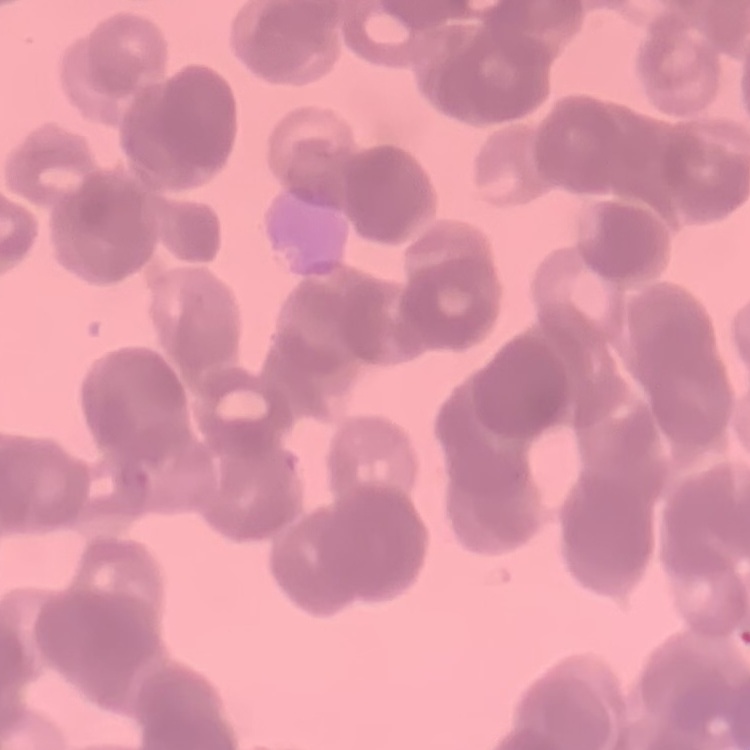
erythrocyte morphology = rouleaux formation
image type = square crop of a larger photomicrograph
stain = Field's or Giemsa
preparation = thin blood film